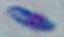
magnification = 1000x
identification = Toxoplasma gondii
modality = micrograph